Give the position of every leukocyte visible.
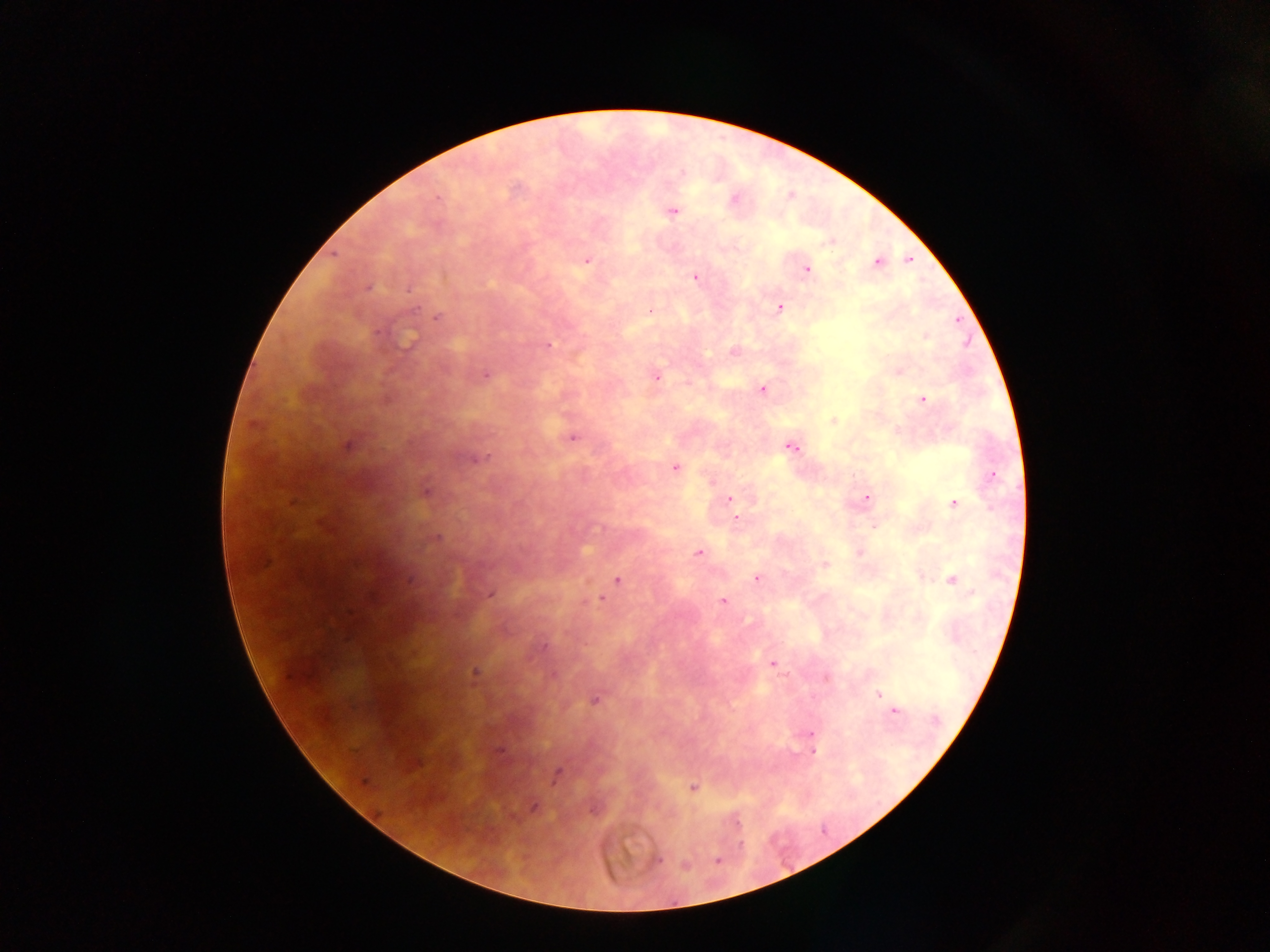

No leukocytes observed.

Approximate centers as x y in pixels.
Summary:
  - Malaria parasite locations: 734 201; 672 210; 586 260; 909 260; 877 262; 806 269; 695 276; 367 287; 779 308; 437 317; 926 336; 546 345; 733 351; 898 371; 485 374; 655 375; 762 389; 923 399; 833 421; 573 437; 348 445; 790 446; 477 458; 674 467; 991 475; 425 490; 867 497; 729 499; 954 502; 735 518; 874 525; 434 537; 698 552; 859 552; 825 564; 757 578; 617 580; 951 580; 490 594; 601 598; 723 600; 772 663; 475 673; 825 676; 878 694; 594 700; 892 711; 811 733; 812 751; 556 772; 693 787; 533 806; 735 822; 656 860; 717 860; 683 865
  - Field of view: single
  - Image size: 1270×952 pixels
  - Capture: mobile-phone photograph through a microscope
  - Preparation: thick blood film
  - Country: Ghana